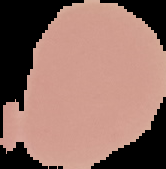

Summary:
  - Image size: 166×169 pixels
  - Preparation: thin blood smear
  - Malaria status: uninfected
  - Image type: segmented cell region on a black background